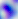
Toxoplasma gondii is shown. Micrograph. Captured at 400x magnification.